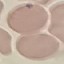
Result: no malaria parasites seen. Cell patch, automatically extracted from a larger field of view and resized to 64 × 64 pixels. Giemsa stain. Thin smear of blood. Acquired by smartphone through the microscope eyepiece.